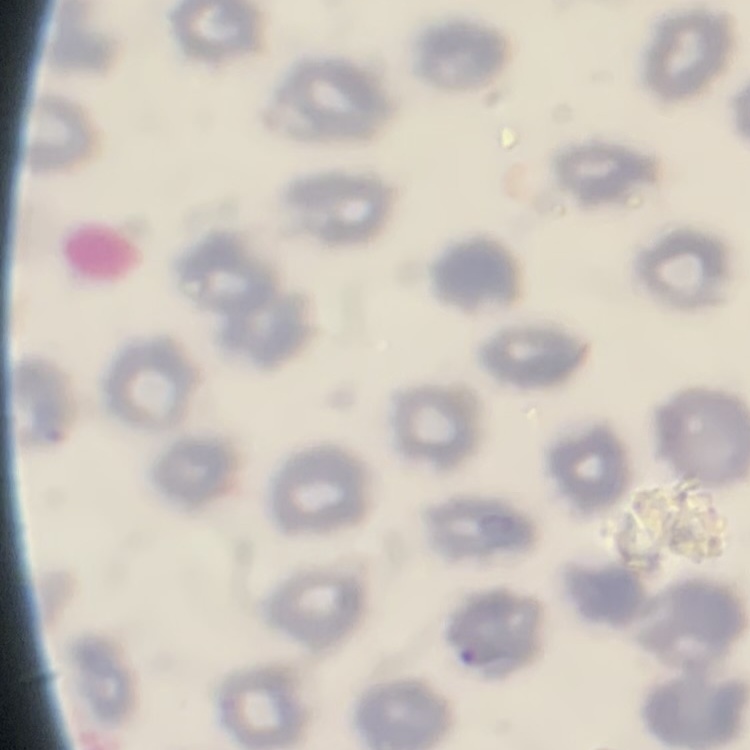

Summary:
  - Erythrocyte morphology: no rouleaux formation
  - Stain: Field's or Giemsa
  - Image type: one tile cut from a larger photomicrograph
  - Preparation: thin blood smear